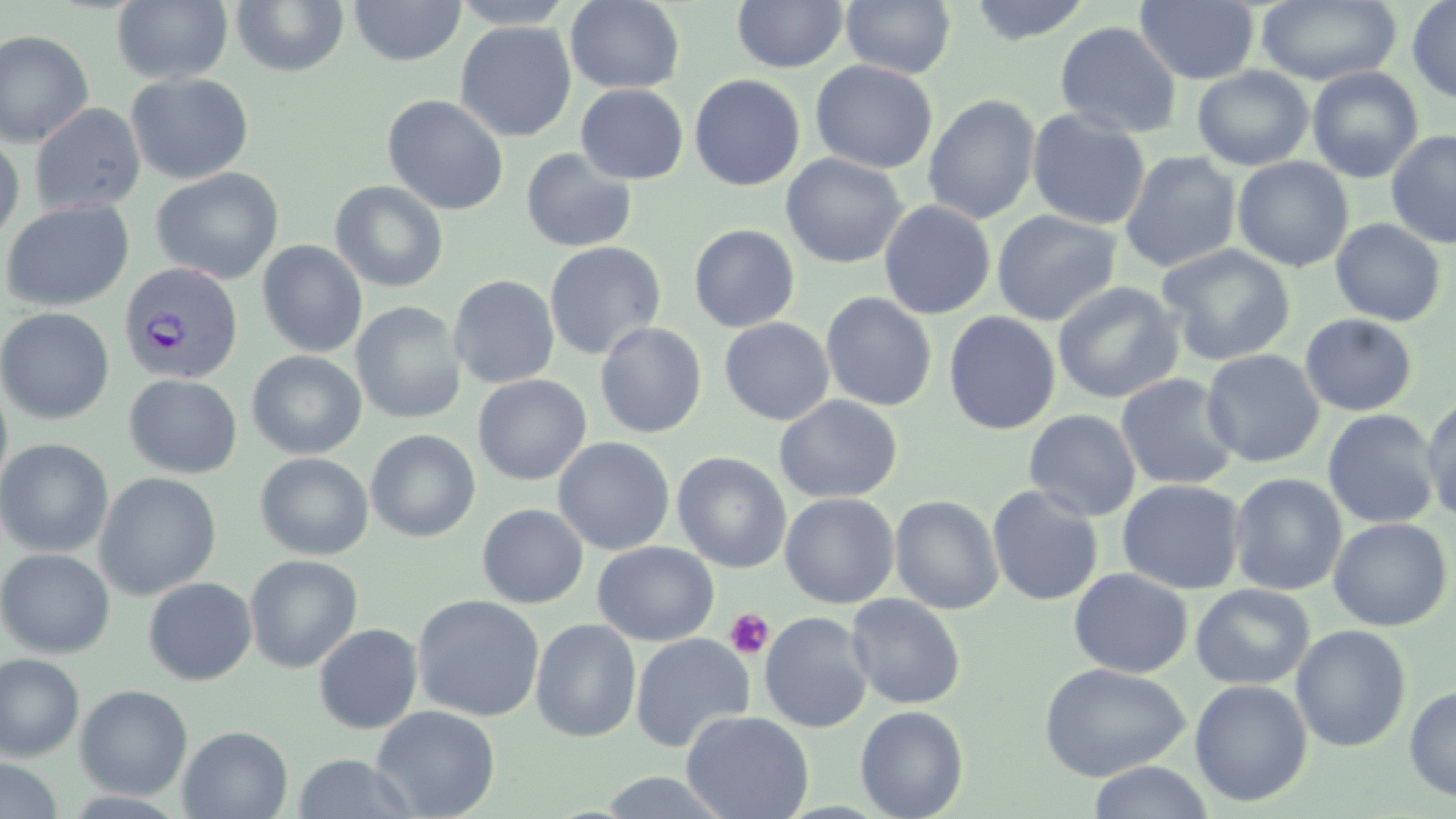
Approximate bounding boxes as (x1, y1, x2, y2) in pixels. Platelet locations: (724, 607, 774, 659). Uninfected red blood cell locations: (448, 0, 577, 29), (731, 0, 848, 73), (967, 0, 1094, 45), (1135, 0, 1259, 85), (1256, 0, 1402, 86), (1407, 0, 1456, 105), (110, 1, 234, 85), (231, 1, 350, 76), (349, 1, 466, 66), (564, 1, 685, 94), (840, 1, 956, 79), (455, 21, 576, 142), (1054, 21, 1181, 139), (0, 29, 94, 147), (811, 60, 938, 174), (1192, 66, 1314, 170), (1307, 66, 1424, 183), (125, 72, 254, 184), (689, 74, 806, 191), (575, 83, 688, 184), (923, 94, 1041, 225), (382, 95, 508, 215), (30, 103, 146, 216), (1026, 109, 1151, 231), (1386, 129, 1455, 249), (0, 134, 25, 247), (521, 147, 637, 253), (1120, 151, 1241, 273), (781, 153, 907, 269), (1232, 157, 1354, 272), (151, 167, 284, 284), (329, 179, 449, 292), (1, 200, 134, 312), (879, 200, 996, 320), (992, 209, 1121, 326), (1330, 218, 1446, 327), (688, 224, 799, 333), (257, 240, 367, 357), (543, 241, 666, 361), (1158, 243, 1296, 367), (449, 275, 560, 389), (1052, 281, 1184, 405), (820, 292, 938, 411), (350, 300, 466, 424), (0, 307, 115, 425), (943, 311, 1061, 435), (1300, 314, 1418, 417), (719, 317, 835, 425), (594, 322, 708, 438), (1201, 349, 1324, 468), (247, 350, 367, 459), (1116, 373, 1241, 491), (124, 374, 242, 479), (473, 374, 591, 486), (0, 378, 14, 498), (774, 395, 902, 504), (1422, 395, 1456, 525), (1322, 408, 1441, 529), (1024, 409, 1141, 521), (365, 429, 481, 543), (553, 436, 676, 555), (0, 439, 113, 558), (672, 451, 792, 573), (255, 453, 373, 559), (94, 471, 222, 600), (1228, 473, 1347, 596), (1117, 479, 1245, 595), (986, 485, 1104, 606), (780, 492, 900, 608), (890, 495, 1004, 615), (477, 503, 589, 608), (1328, 517, 1453, 631), (593, 541, 718, 646), (1, 548, 115, 658), (245, 554, 363, 673), (1068, 567, 1193, 678), (143, 578, 257, 685), (1191, 583, 1315, 690), (412, 594, 545, 722), (846, 594, 966, 709), (759, 611, 873, 733), (530, 618, 642, 743), (313, 623, 423, 734), (631, 623, 872, 739), (1290, 625, 1412, 752), (630, 633, 756, 752), (0, 654, 84, 762), (1038, 662, 1191, 782), (1190, 679, 1312, 806), (75, 685, 193, 801), (1404, 685, 1456, 802), (371, 705, 500, 819), (855, 705, 969, 819), (681, 710, 814, 819), (178, 725, 293, 818), (291, 753, 421, 818), (0, 758, 64, 819), (1086, 761, 1216, 819), (594, 770, 734, 817). Plasmodium vivax-infected red blood cell locations: (119, 262, 243, 384). Slide-level diagnosis: Plasmodium vivax. May-Grünwald-Giemsa stain. Image is 1456×819 pixels. Single field of view. Optical microscopy. Thin blood smear. 1000x magnification.